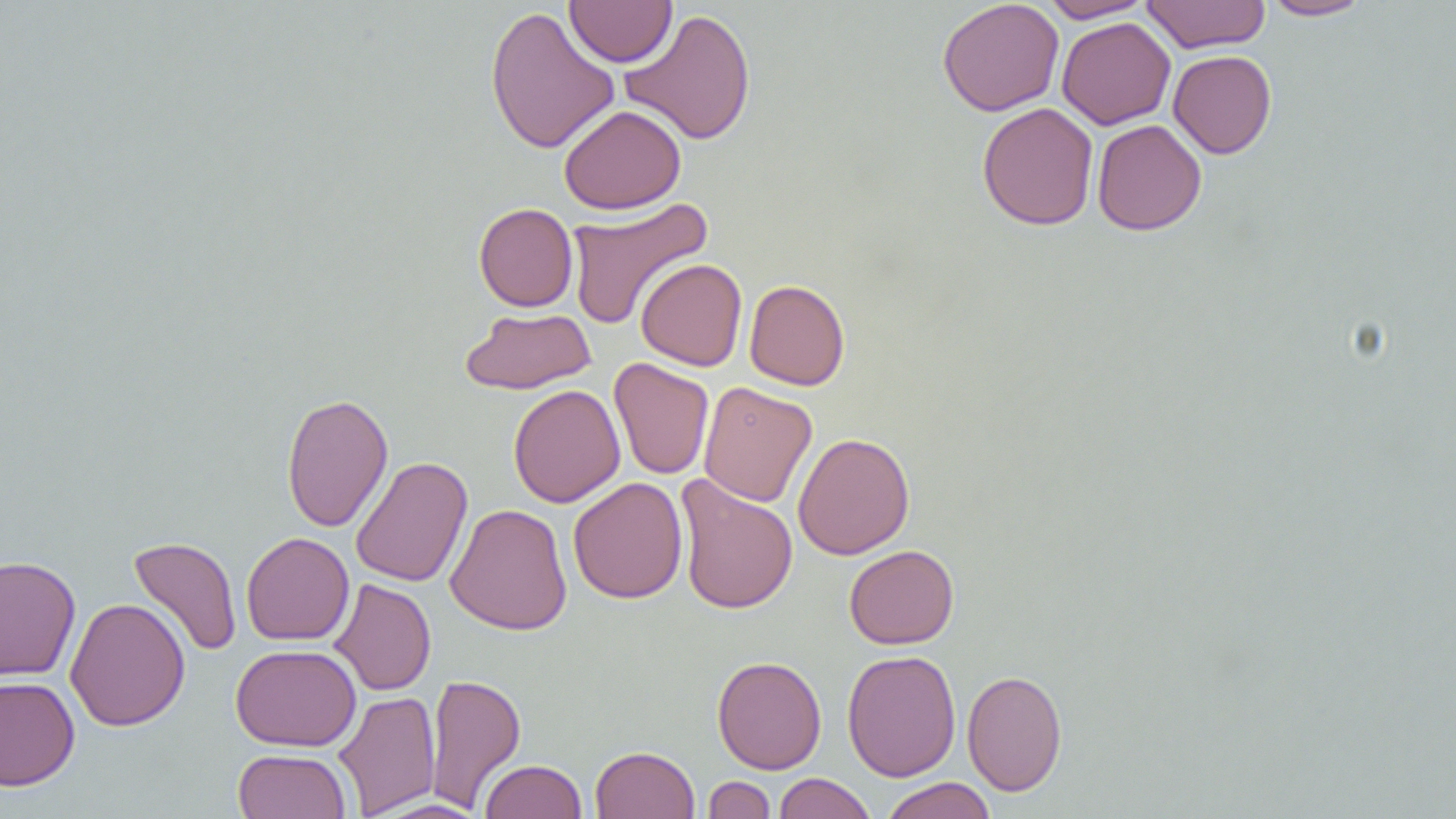 Approximate bounding boxes as named x1/y1/x2/y2 corners in pixels. Uninfected red blood cell locations: (x1=564, y1=0, x2=678, y2=67), (x1=937, y1=0, x2=1064, y2=116), (x1=1039, y1=0, x2=1155, y2=22), (x1=1140, y1=0, x2=1271, y2=53), (x1=1259, y1=0, x2=1374, y2=21), (x1=483, y1=5, x2=620, y2=155), (x1=620, y1=8, x2=758, y2=145), (x1=1056, y1=16, x2=1176, y2=130), (x1=1167, y1=50, x2=1277, y2=159), (x1=976, y1=102, x2=1099, y2=231), (x1=559, y1=104, x2=686, y2=214), (x1=1091, y1=119, x2=1206, y2=236), (x1=564, y1=197, x2=713, y2=331), (x1=474, y1=202, x2=578, y2=311), (x1=635, y1=258, x2=747, y2=371), (x1=744, y1=279, x2=850, y2=391), (x1=460, y1=307, x2=596, y2=395), (x1=609, y1=358, x2=714, y2=480), (x1=698, y1=381, x2=817, y2=508), (x1=508, y1=384, x2=625, y2=508), (x1=281, y1=392, x2=393, y2=533), (x1=793, y1=432, x2=915, y2=560), (x1=350, y1=456, x2=472, y2=588), (x1=674, y1=475, x2=798, y2=615), (x1=568, y1=476, x2=688, y2=604), (x1=445, y1=503, x2=572, y2=635), (x1=241, y1=532, x2=354, y2=646), (x1=128, y1=536, x2=242, y2=657), (x1=844, y1=545, x2=959, y2=649), (x1=0, y1=554, x2=81, y2=682), (x1=328, y1=578, x2=436, y2=696), (x1=65, y1=597, x2=191, y2=732), (x1=230, y1=643, x2=361, y2=751), (x1=842, y1=649, x2=961, y2=782), (x1=712, y1=655, x2=826, y2=774), (x1=962, y1=669, x2=1067, y2=797), (x1=425, y1=671, x2=526, y2=812), (x1=0, y1=676, x2=80, y2=791), (x1=333, y1=691, x2=441, y2=817), (x1=589, y1=745, x2=700, y2=819), (x1=233, y1=748, x2=352, y2=819), (x1=479, y1=759, x2=587, y2=818), (x1=773, y1=772, x2=877, y2=819), (x1=702, y1=776, x2=776, y2=818), (x1=880, y1=777, x2=997, y2=819), (x1=367, y1=797, x2=490, y2=818). Slide-level diagnosis: no evidence of blood parasites. Captured at 1000x magnification. Single field of view. Light microscopy. Image is 1456×819 pixels. Thin blood smear.